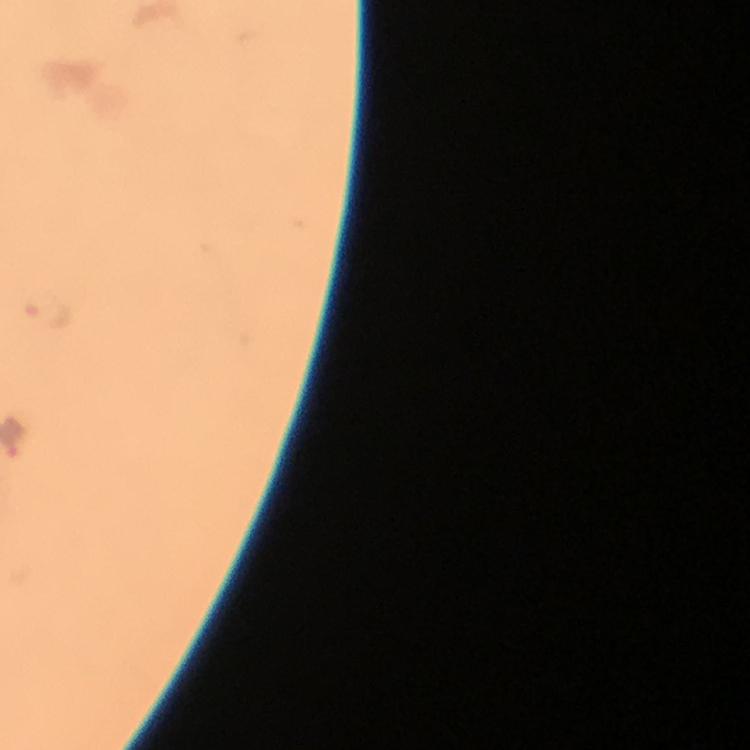

Approximate centers as (x, y) in pixels. Malaria parasite locations: (51, 313). At 100x magnification. Giemsa stain. A crop from one field of view. Immersion oil applied. Photographed through the microscope with a smartphone camera. From a malaria diagnostic workup. Image is 750×750 pixels. Thick blood film.